Classify this cell by malaria status.
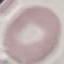
It is uninfected.

Summary:
  - Stain: Giemsa
  - Preparation: thin blood film
  - Image type: cell patch, automatically extracted from a larger field of view and resized to 64 × 64 pixels
  - Capture: smartphone through the microscope eyepiece